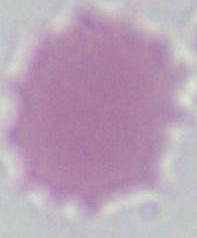
Summary:
  - Identification: red blood cell
  - Magnification: 1000x
  - Modality: photomicrograph